Locate every Plasmodium parasite.
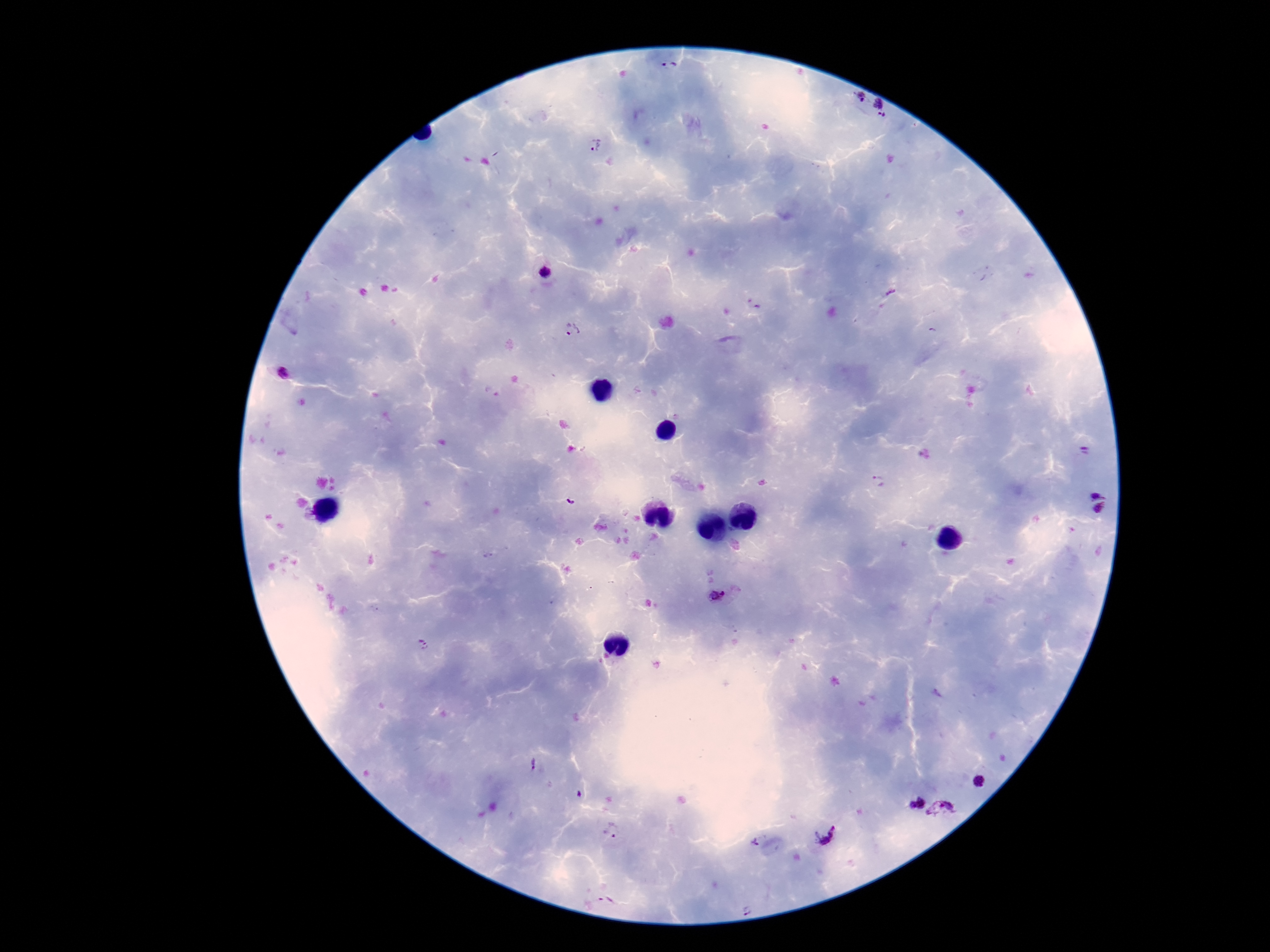

Approximate centers as [x, y] in pixels.
Plasmodium parasites: [670, 67], [862, 96], [880, 104], [881, 117], [596, 145], [546, 270], [754, 304], [571, 329], [284, 372], [1086, 451], [878, 481], [1098, 492], [571, 501], [1100, 510], [718, 595], [423, 644], [534, 766], [981, 783], [913, 801], [944, 810], [612, 830], [826, 834], [756, 842], [605, 899], [748, 911].

Image is 1270×952 pixels. Single field of view. Thick peripheral-blood smear. 100x magnification. Patient malaria status: infected. Giemsa stain. Smartphone photograph taken through the microscope eyepiece.